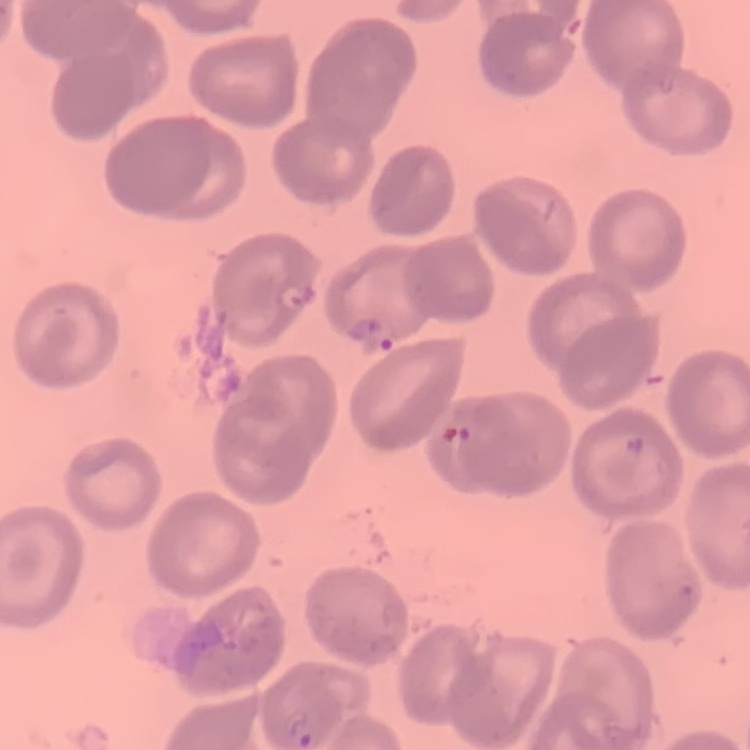

{
  "erythrocyte_morphology": "no rouleaux formation",
  "preparation": "thin peripheral smear",
  "image_type": "one tile cut from a larger photomicrograph",
  "stain": "Field's or Giemsa"
}